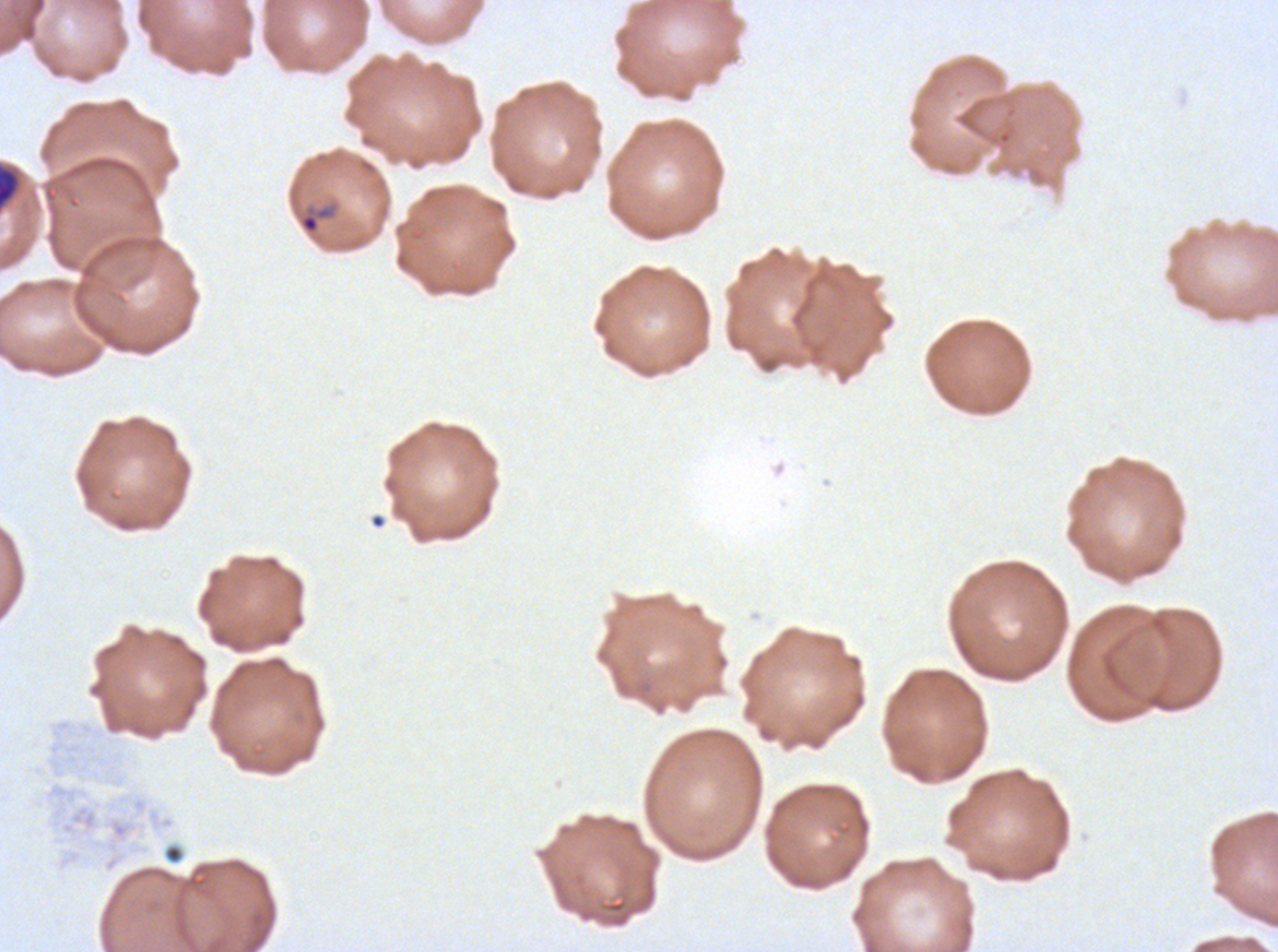
Approximate bounding boxes as (x1, y1, x2, y2) in pixels. Early schizont locations: (0, 168, 18, 208). Ring locations: (298, 204, 335, 235). Ex-vivo P. falciparum culture from a patient in The Gambia, grown for 24 to 48 hours. Image is 1278×952 pixels. A sub-image separated from a larger composite. Giemsa-stained preparation. Thin blood smear. Life-cycle stages observed: ring, early schizont.